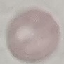

Result: no malaria parasites seen. Photographed with a smartphone camera at the microscope eyepiece. Giemsa-stained preparation. Cell patch, automatically extracted from a larger field of view and resized to 64 × 64 pixels. Thin smear of blood.